Describe the morphology of the red blood cells.
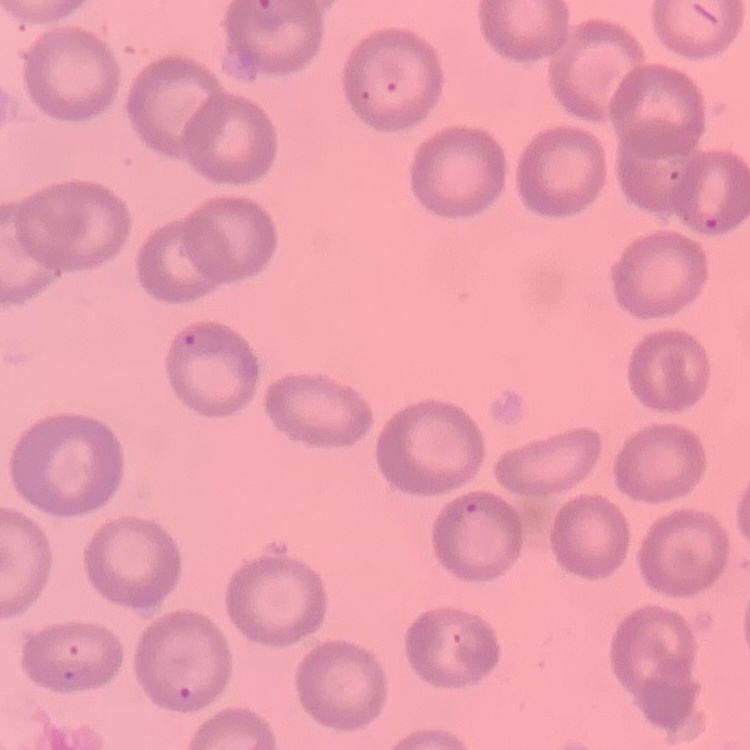

They show no rouleaux formation.

Summary:
  - Stain: Field's or Giemsa
  - Preparation: thin blood film
  - Image type: one tile cut from a larger photomicrograph